Locate every blood parasite and identify its species.
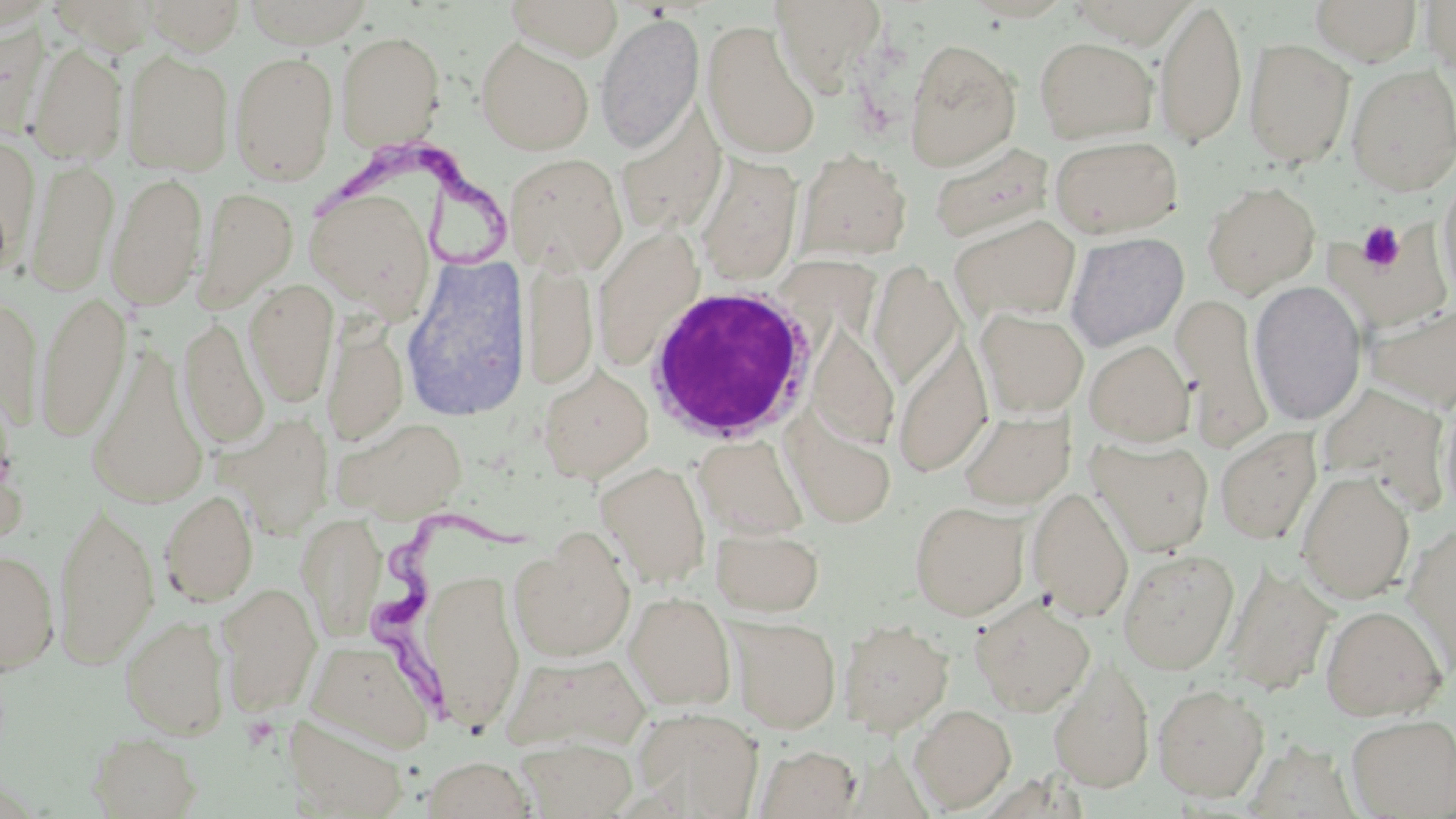

Approximate bounding boxes as (x1, y1, x2, y2) in pixels.
Trypanosoma brucei: (316, 147, 525, 270), (374, 510, 534, 729).
No Plasmodium falciparum, Plasmodium ovale, Plasmodium malariae, Plasmodium vivax, or Babesia divergens observed.

White blood cell locations: (641, 283, 816, 446). Platelet locations: (1357, 220, 1406, 273), (241, 716, 278, 751). Uninfected red blood cell locations: (143, 0, 246, 55), (240, 0, 376, 48), (504, 0, 624, 60), (769, 0, 888, 94), (1154, 0, 1247, 149), (1309, 0, 1423, 65), (49, 1, 161, 56), (1421, 1, 1455, 78), (595, 12, 704, 154), (702, 18, 820, 160), (0, 19, 50, 136), (335, 31, 446, 150), (1034, 36, 1157, 144), (476, 37, 594, 155), (903, 37, 1022, 170), (1243, 37, 1355, 168), (27, 43, 128, 165), (122, 50, 234, 176), (229, 50, 339, 186), (1346, 63, 1456, 196), (615, 102, 728, 238), (1050, 134, 1184, 237), (0, 135, 39, 269), (928, 142, 1055, 243), (794, 148, 913, 263), (505, 151, 627, 276), (694, 153, 804, 285), (26, 157, 119, 297), (1437, 169, 1456, 307), (107, 170, 208, 310), (1202, 180, 1320, 297), (194, 186, 298, 313), (306, 187, 437, 318), (950, 214, 1082, 323), (1339, 225, 1452, 331), (1065, 231, 1189, 351), (400, 254, 532, 422), (522, 256, 598, 389), (870, 262, 963, 391), (244, 279, 339, 406), (1249, 280, 1367, 426), (34, 291, 131, 442), (1173, 291, 1272, 450), (0, 293, 44, 431), (1365, 302, 1456, 414), (975, 307, 1089, 418), (179, 316, 269, 449), (322, 319, 409, 445), (807, 320, 899, 449), (892, 334, 993, 476), (1084, 340, 1194, 445), (87, 344, 210, 509), (538, 365, 654, 482), (1317, 381, 1451, 511), (1439, 389, 1456, 520), (957, 408, 1076, 510), (784, 409, 896, 528), (222, 412, 334, 538), (333, 415, 468, 521), (1215, 428, 1321, 544), (693, 434, 808, 540), (1088, 436, 1214, 555), (597, 460, 711, 587), (1296, 470, 1415, 604), (1026, 485, 1134, 621), (160, 489, 258, 607), (52, 500, 159, 669), (909, 500, 1030, 621), (296, 512, 387, 641), (1403, 522, 1456, 673), (711, 524, 825, 617), (507, 531, 637, 663), (0, 548, 60, 674), (1117, 548, 1239, 675), (1223, 562, 1337, 696), (419, 567, 526, 732), (216, 581, 322, 716), (623, 590, 737, 710), (972, 595, 1095, 716), (1319, 604, 1449, 720), (120, 615, 231, 740), (729, 616, 841, 733), (839, 618, 954, 736), (307, 638, 436, 751), (503, 653, 651, 752), (1048, 657, 1155, 791), (1152, 683, 1269, 801), (908, 703, 1016, 813), (631, 708, 763, 817), (282, 714, 409, 818), (1346, 714, 1456, 817), (88, 732, 201, 818), (516, 736, 638, 818), (755, 744, 862, 818), (421, 755, 536, 818). Slide-level diagnosis: Trypanosoma brucei. 1000x magnification. May-Grünwald-Giemsa-stained preparation. Optical microscopy. Thin blood film. Image is 1456×819 pixels. One field of a larger specimen.